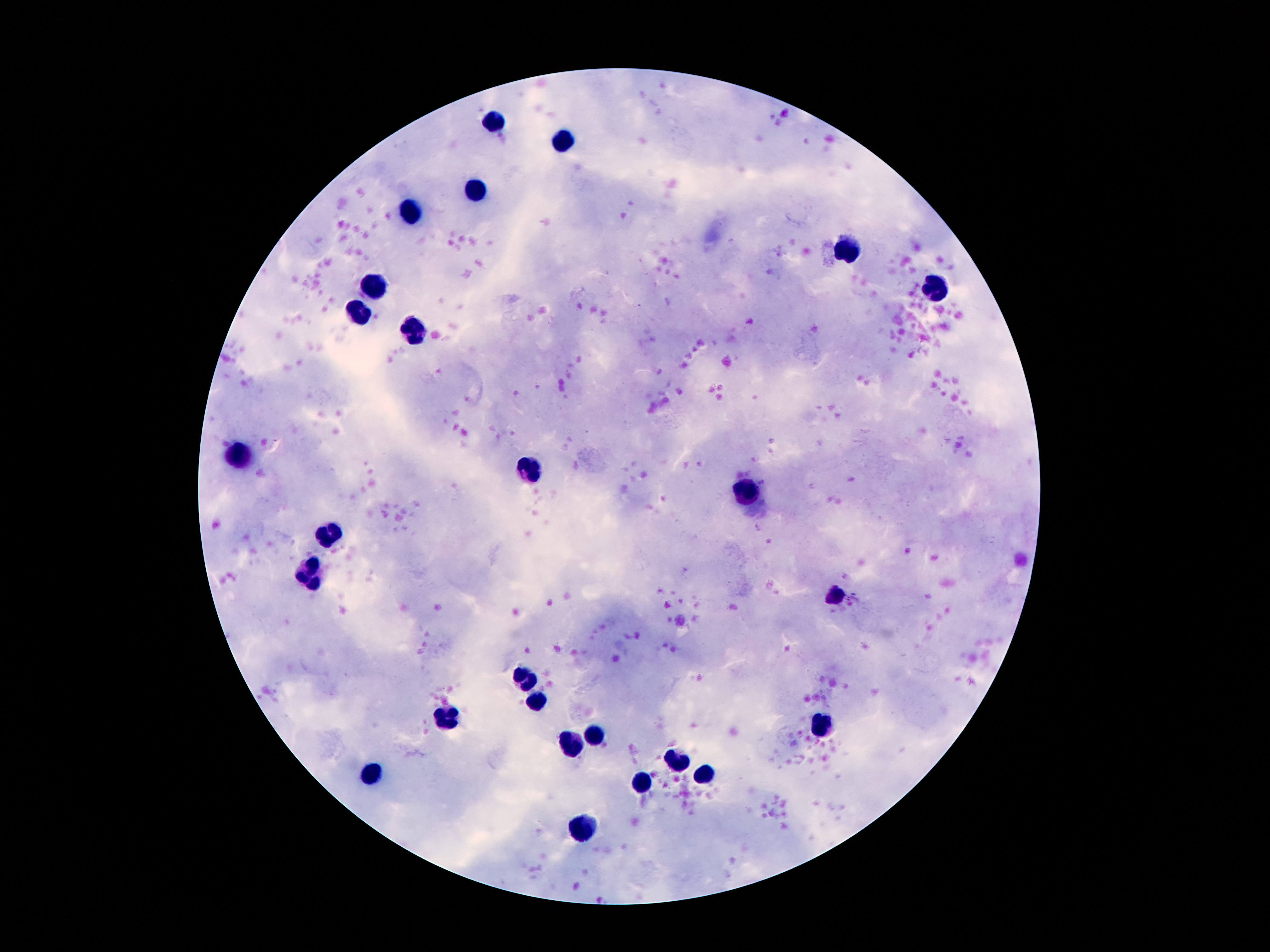

leukocyte locations = approximate object centers, in pixels from the top-left corner: (x=494, y=117), (x=562, y=142), (x=476, y=190), (x=412, y=212), (x=850, y=248), (x=373, y=287), (x=934, y=288), (x=357, y=309), (x=410, y=331), (x=238, y=453), (x=527, y=471), (x=744, y=490), (x=330, y=533), (x=312, y=574), (x=836, y=597), (x=521, y=681), (x=535, y=701), (x=445, y=716), (x=824, y=726), (x=592, y=736), (x=572, y=747), (x=676, y=759), (x=371, y=771), (x=703, y=774), (x=641, y=780), (x=582, y=828)
capture = smartphone camera through the microscope eyepiece
field of view = one from this slide
stain = Giemsa
image size = 1270×952 pixels
magnification = 100x
patient malaria status = uninfected
preparation = thick blood smear